Identify the blood parasite species.
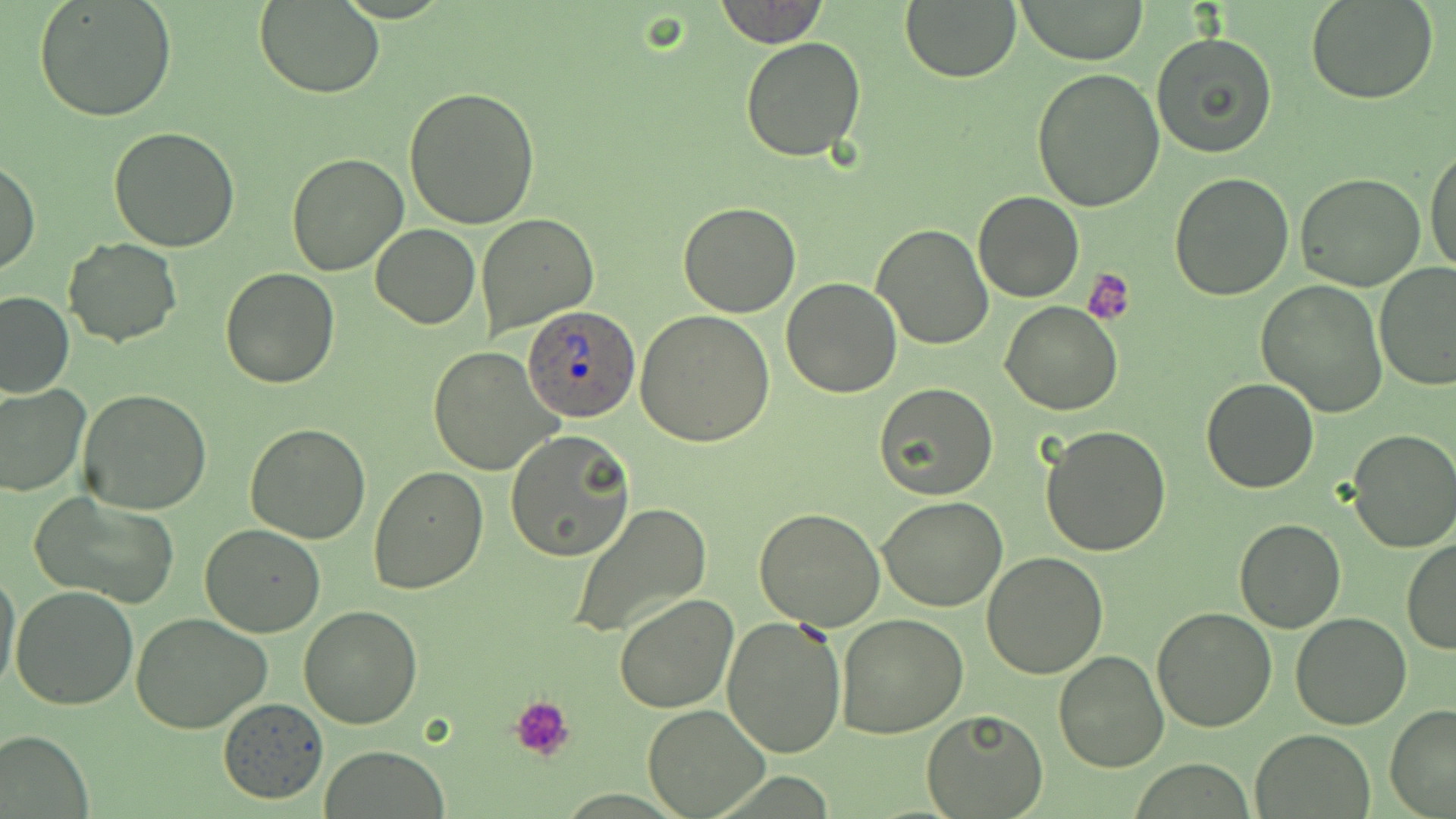
Plasmodium ovale.

Approximate bounding boxes as (x1, y1, x2, y2) in pixels. Platelet locations: (1082, 268, 1136, 326), (510, 695, 574, 761). Uninfected red blood cell locations: (35, 0, 178, 123), (714, 0, 828, 48), (899, 0, 1020, 84), (1014, 0, 1149, 65), (1305, 0, 1439, 104), (255, 1, 385, 99), (1151, 30, 1279, 159), (739, 36, 866, 162), (1032, 69, 1165, 215), (404, 86, 541, 230), (108, 125, 240, 251), (1425, 143, 1456, 278), (286, 152, 411, 276), (0, 156, 39, 277), (1169, 172, 1294, 301), (1296, 173, 1427, 293), (974, 192, 1082, 302), (677, 200, 801, 318), (476, 214, 598, 334), (871, 223, 996, 351), (372, 224, 479, 328), (64, 237, 181, 347), (1372, 262, 1456, 391), (220, 267, 340, 388), (781, 276, 902, 398), (1256, 281, 1388, 416), (0, 291, 75, 399), (1001, 303, 1121, 416), (634, 308, 775, 447), (428, 347, 562, 476), (1201, 377, 1320, 493), (874, 382, 998, 501), (0, 384, 89, 497), (77, 389, 212, 516), (245, 423, 370, 544), (1040, 423, 1170, 557), (1347, 428, 1456, 553), (505, 431, 635, 561), (367, 466, 489, 593), (29, 489, 180, 607), (876, 496, 1006, 612), (567, 503, 713, 639), (754, 507, 887, 630), (1233, 520, 1347, 632), (200, 523, 326, 637), (1402, 539, 1456, 655), (982, 553, 1109, 678), (0, 564, 21, 697), (10, 585, 138, 711), (613, 593, 739, 713), (297, 606, 424, 730), (1152, 606, 1276, 732), (1290, 612, 1412, 730), (129, 613, 272, 734), (837, 614, 969, 738), (722, 616, 849, 758), (1053, 650, 1170, 773), (218, 697, 329, 803), (643, 704, 769, 817), (1385, 705, 1456, 817), (921, 708, 1049, 819), (0, 728, 94, 818), (1252, 729, 1375, 818), (321, 744, 450, 817). Plasmodium ovale-infected red blood cell locations: (522, 304, 640, 423). Image is 1456×819 pixels. Thin blood smear. 1000x magnification. Single field of view. Optical microscopy. May-Grünwald-Giemsa stain.